Assess this cell for malaria.
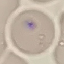
Uninfected.

Giemsa stain. Photographed with a smartphone camera at the microscope eyepiece. Automatically extracted cell patch, resized to 64 × 64 pixels. Thin smear of blood.